Locate every blood parasite and identify its species.
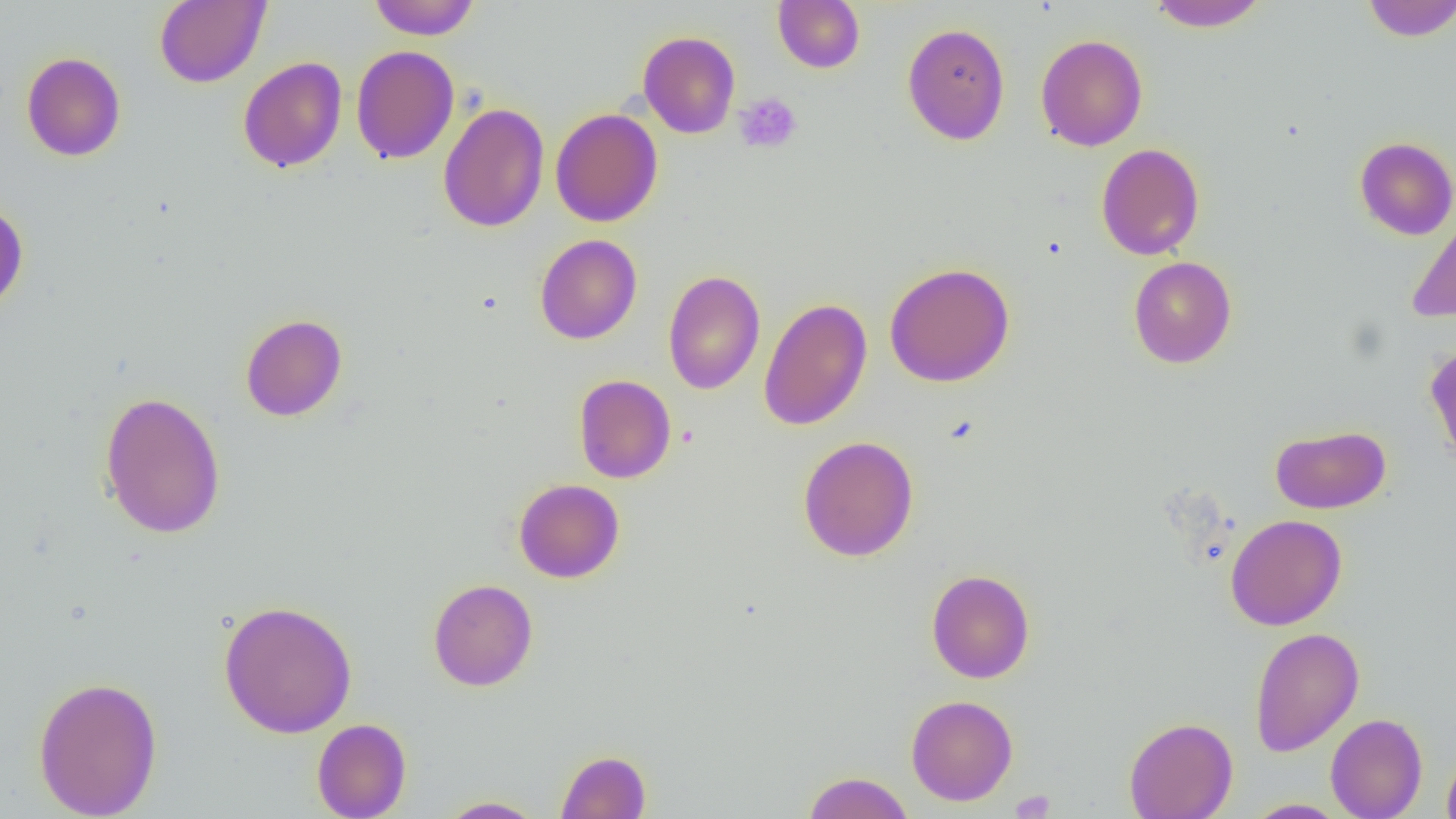

No blood parasites seen.

slide-level diagnosis = no evidence of blood parasites
modality = light microscopy
platelet locations = approximate bounding boxes as named x1/y1/x2/y2 corners in pixels: (x1=734, y1=92, x2=801, y2=154), (x1=1011, y1=790, x2=1057, y2=818)
field of view = one of a larger specimen
preparation = thin blood smear
uninfected red blood cell locations = approximate bounding boxes as named x1/y1/x2/y2 corners in pixels: (x1=154, y1=0, x2=270, y2=88), (x1=368, y1=0, x2=481, y2=40), (x1=1146, y1=0, x2=1269, y2=31), (x1=1360, y1=0, x2=1456, y2=42), (x1=772, y1=1, x2=865, y2=73), (x1=901, y1=22, x2=1011, y2=145), (x1=638, y1=31, x2=740, y2=139), (x1=1035, y1=34, x2=1148, y2=151), (x1=351, y1=45, x2=459, y2=164), (x1=21, y1=52, x2=126, y2=161), (x1=238, y1=57, x2=347, y2=172), (x1=438, y1=102, x2=549, y2=232), (x1=550, y1=108, x2=663, y2=227), (x1=1354, y1=136, x2=1456, y2=240), (x1=1096, y1=143, x2=1205, y2=260), (x1=0, y1=198, x2=29, y2=314), (x1=1406, y1=209, x2=1456, y2=322), (x1=535, y1=234, x2=642, y2=344), (x1=1128, y1=256, x2=1237, y2=369), (x1=884, y1=262, x2=1015, y2=387), (x1=663, y1=269, x2=765, y2=394), (x1=758, y1=297, x2=872, y2=431), (x1=240, y1=313, x2=348, y2=422), (x1=1424, y1=343, x2=1456, y2=465), (x1=573, y1=374, x2=677, y2=483), (x1=99, y1=390, x2=227, y2=540), (x1=1270, y1=424, x2=1390, y2=514), (x1=797, y1=436, x2=919, y2=562), (x1=513, y1=478, x2=625, y2=583), (x1=1225, y1=514, x2=1347, y2=630), (x1=926, y1=569, x2=1035, y2=683), (x1=428, y1=578, x2=538, y2=691), (x1=218, y1=599, x2=358, y2=738), (x1=1249, y1=626, x2=1364, y2=757), (x1=32, y1=675, x2=163, y2=819), (x1=906, y1=694, x2=1018, y2=806), (x1=1325, y1=713, x2=1428, y2=819), (x1=1123, y1=716, x2=1237, y2=819), (x1=312, y1=718, x2=411, y2=819), (x1=1441, y1=746, x2=1456, y2=819), (x1=555, y1=749, x2=652, y2=819), (x1=802, y1=771, x2=914, y2=818), (x1=437, y1=796, x2=547, y2=818), (x1=1243, y1=799, x2=1350, y2=818)
image size = 1456×819 pixels
magnification = 1000x